Locate every blood parasite and identify its species.
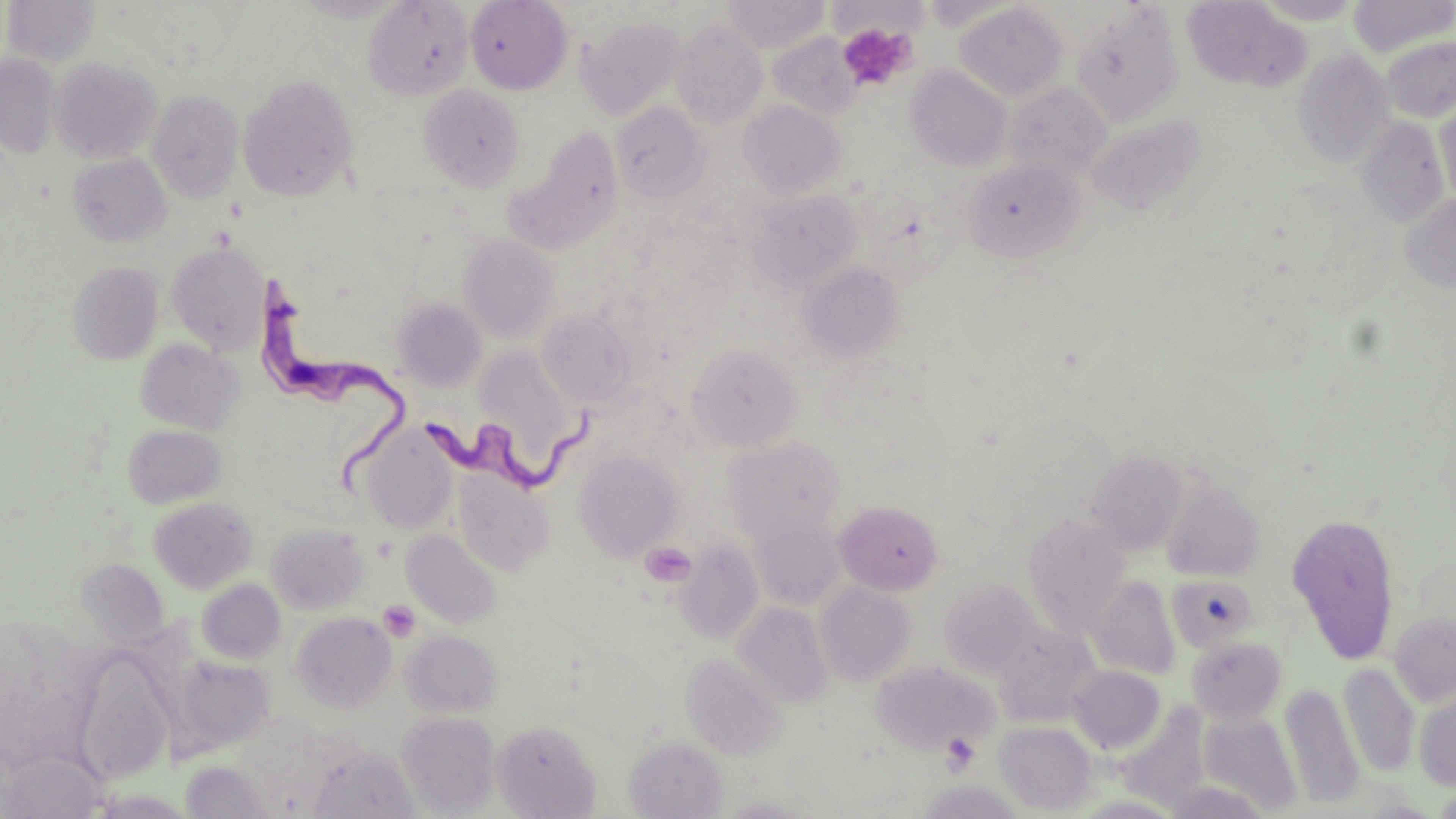

Approximate bounding boxes as (x1,y1)-(x2,y2) corner pairs in pixels.
Trypanosoma brucei: (252,275)-(408,495), (424,391)-(602,493).
No Plasmodium falciparum, Plasmodium ovale, Plasmodium malariae, Plasmodium vivax, or Babesia divergens observed.

slide-level diagnosis = Trypanosoma brucei
stain = May-Grünwald-Giemsa
field of view = one of a larger specimen
preparation = thin blood smear
uninfected red blood cell locations = approximate bounding boxes as (x1,y1)-(x2,y2) corner pairs in pixels: (288,0)-(412,23), (465,0)-(572,95), (722,0)-(830,52), (1182,0)-(1312,93), (1250,0)-(1368,25), (1348,0)-(1455,58), (2,1)-(102,67), (363,1)-(474,100), (954,2)-(1070,103), (1070,4)-(1185,128), (578,16)-(687,121), (670,21)-(769,130), (767,33)-(862,120), (1380,36)-(1456,124), (1291,48)-(1396,169), (0,55)-(60,159), (51,57)-(162,163), (905,66)-(1012,171), (238,74)-(359,202), (1002,81)-(1112,182), (419,85)-(524,191), (146,90)-(243,203), (1434,93)-(1455,210), (738,100)-(847,199), (611,102)-(710,204), (1086,111)-(1210,219), (1353,118)-(1452,228), (511,127)-(624,250), (66,153)-(171,247), (962,157)-(1084,262), (745,188)-(863,293), (1400,194)-(1456,294), (459,235)-(559,343), (166,242)-(270,354), (67,262)-(163,365), (798,262)-(904,362), (392,299)-(487,392), (538,311)-(637,409), (135,338)-(246,435), (686,343)-(803,451), (472,346)-(581,474), (357,423)-(459,534), (122,424)-(227,510), (724,437)-(846,543), (1086,449)-(1188,556), (574,451)-(683,561), (453,470)-(554,576), (1160,477)-(1266,583), (148,496)-(258,594), (835,499)-(943,595), (748,510)-(844,609), (1285,511)-(1402,665), (1023,514)-(1131,635), (266,522)-(370,615), (402,530)-(503,629), (675,541)-(764,644), (76,559)-(168,646), (1166,574)-(1259,652), (1087,575)-(1181,680), (196,579)-(286,664), (939,580)-(1043,679), (815,582)-(916,686), (732,603)-(833,708), (290,612)-(397,713), (1388,612)-(1456,706), (993,626)-(1099,727), (401,630)-(502,717), (1186,636)-(1288,724), (681,653)-(788,760), (72,654)-(175,785), (171,656)-(276,755), (870,660)-(999,754), (1338,663)-(1420,778), (1068,665)-(1166,754), (1281,683)-(1364,810), (1414,689)-(1456,791), (1200,710)-(1303,813), (396,711)-(500,817), (232,716)-(335,813), (492,720)-(601,818), (994,721)-(1097,815), (625,737)-(727,818), (306,745)-(422,819), (1,752)-(110,819), (180,761)-(279,818), (1159,780)-(1276,819), (1433,787)-(1456,818), (85,789)-(196,818)
image size = 1456×819 pixels
magnification = 1000x
platelet locations = approximate bounding boxes as (x1,y1)-(x2,y2) corner pairs in pixels: (837,22)-(915,90), (641,541)-(696,586), (377,600)-(420,641), (941,734)-(980,772)
modality = optical microscopy